Locate and identify every blood parasite.
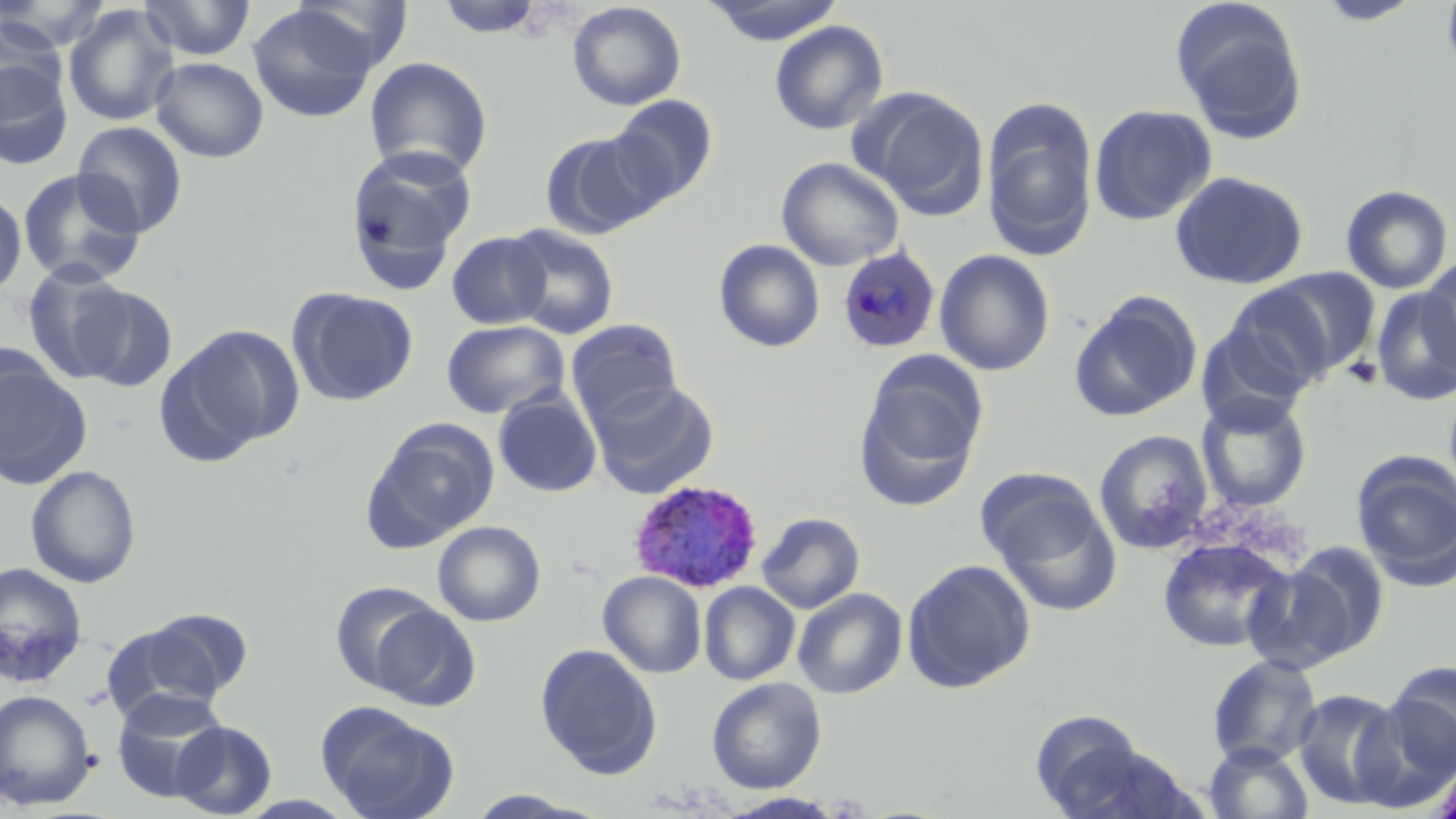
Approximate bounding boxes as [x1, y1, x2, y2] in pixels.
Plasmodium ovale-infected red blood cells: [836, 244, 941, 354], [628, 479, 764, 593].
No Plasmodium falciparum, Plasmodium malariae, Plasmodium vivax, Babesia divergens, or Trypanosoma brucei observed.

slide-level diagnosis = Plasmodium ovale
stain = May-Grünwald-Giemsa
uninfected red blood cell locations = approximate bounding boxes as [x1, y1, x2, y2] in pixels: [139, 0, 257, 61], [291, 0, 415, 73], [435, 0, 545, 39], [1314, 0, 1425, 26], [1441, 0, 1456, 84], [1, 1, 112, 54], [566, 1, 686, 111], [703, 1, 845, 45], [1171, 1, 1310, 145], [62, 4, 180, 127], [247, 4, 378, 123], [0, 14, 68, 117], [770, 20, 888, 136], [364, 56, 493, 179], [0, 57, 75, 170], [151, 57, 269, 163], [858, 89, 990, 219], [609, 94, 719, 205], [981, 99, 1099, 261], [1089, 104, 1217, 225], [72, 121, 188, 237], [539, 130, 662, 239], [344, 148, 476, 287], [776, 156, 904, 271], [18, 168, 147, 287], [1169, 170, 1309, 290], [1340, 185, 1453, 294], [0, 188, 26, 302], [503, 224, 620, 340], [446, 232, 551, 330], [713, 239, 825, 352], [935, 249, 1055, 376], [1419, 257, 1455, 375], [21, 261, 135, 383], [1260, 267, 1382, 378], [1218, 284, 1342, 398], [75, 285, 178, 393], [288, 287, 418, 407], [1371, 288, 1456, 405], [1068, 291, 1202, 422], [566, 319, 682, 425], [441, 320, 569, 419], [157, 324, 301, 461], [0, 353, 92, 489], [855, 361, 985, 510], [588, 379, 719, 499], [493, 390, 602, 497], [1196, 393, 1312, 512], [362, 419, 499, 551], [1094, 430, 1214, 554], [1351, 452, 1456, 588], [25, 465, 141, 588], [989, 489, 1122, 615], [757, 512, 865, 614], [433, 521, 546, 626], [1157, 537, 1294, 653], [1270, 542, 1390, 665], [901, 559, 1036, 693], [0, 562, 89, 688], [598, 571, 707, 677], [330, 580, 448, 693], [699, 581, 800, 685], [792, 588, 908, 699], [366, 602, 481, 711], [101, 619, 237, 725], [535, 643, 662, 779], [1207, 654, 1323, 766], [1384, 661, 1456, 779], [706, 676, 827, 794], [110, 688, 230, 802], [0, 689, 97, 810], [1292, 690, 1407, 810], [317, 703, 460, 819], [1029, 712, 1175, 818], [169, 720, 278, 818], [1203, 741, 1314, 819], [1430, 756, 1456, 819], [464, 790, 604, 818], [721, 792, 846, 818]
field of view = single
platelet locations = approximate bounding boxes as [x1, y1, x2, y2] in pixels: [1342, 356, 1383, 390]
image size = 1456×819 pixels
magnification = 1000x
modality = optical microscopy
preparation = thin blood film